Classify this cell by malaria status.
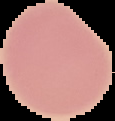

It is uninfected.

Cell region segmented out of the field of view; the surrounding area is masked to black. Image is 115×121 pixels. From a thin blood film.